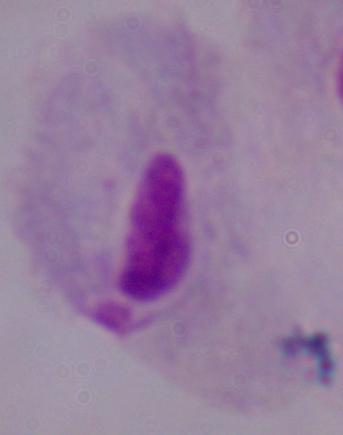

Summary:
  - Identification: trichomonad
  - Magnification: 1000x
  - Modality: photomicrograph